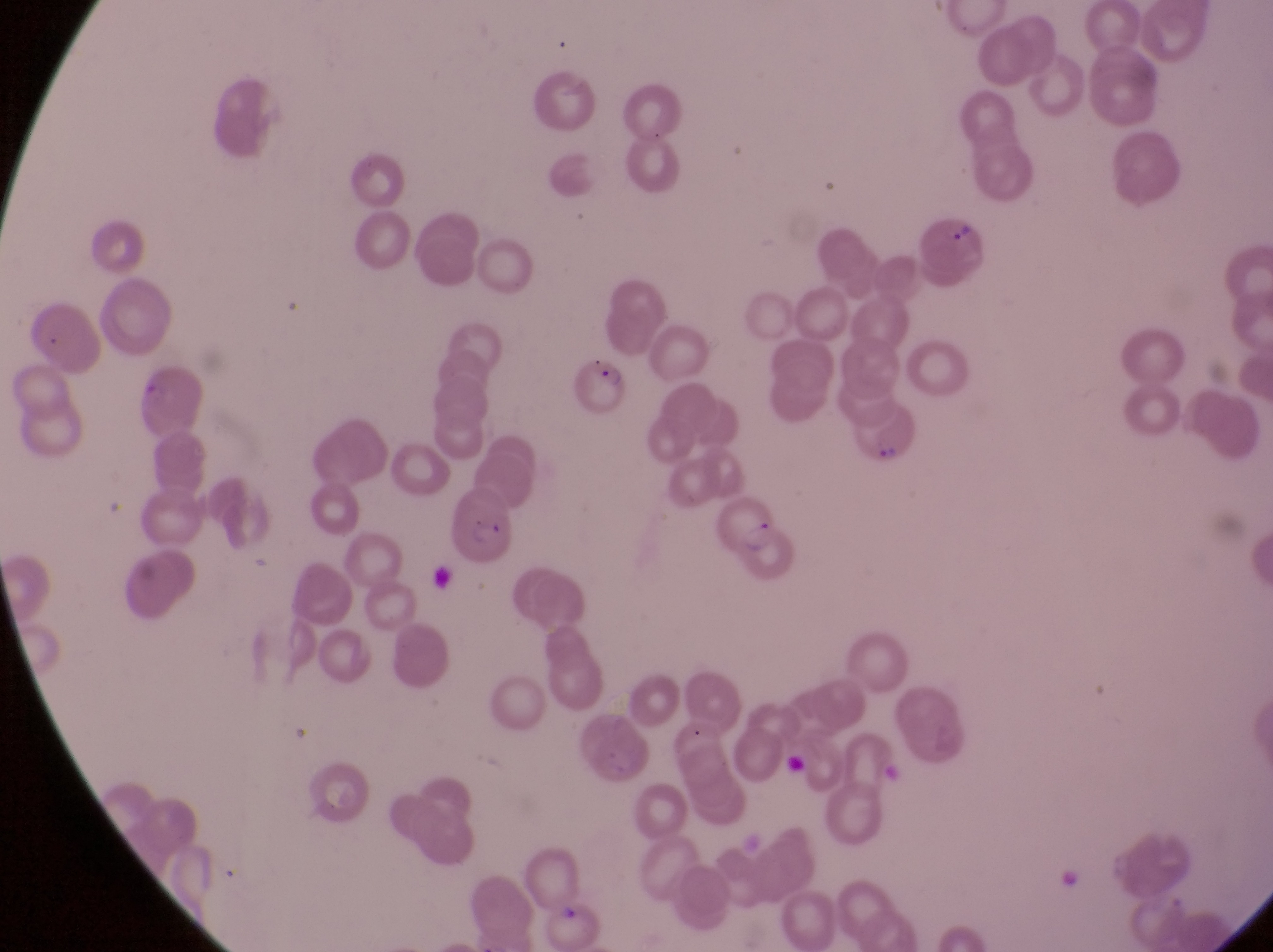
Approximate bounding boxes as [left, top, right, bottom] in pixels.
Summary:
  - Parasitised red blood cell locations: [913, 215, 985, 275], [574, 352, 632, 410], [856, 400, 918, 468], [445, 489, 515, 559], [714, 495, 799, 583]
  - Capture: smartphone photograph through the eyepiece of an Olympus CX-23 microscope
  - Preparation: thin blood film
  - Image size: 1273×952 pixels
  - Magnification: 1000x
  - Country: Uganda
  - Field of view: single